Give the position of every leukocyte visible.
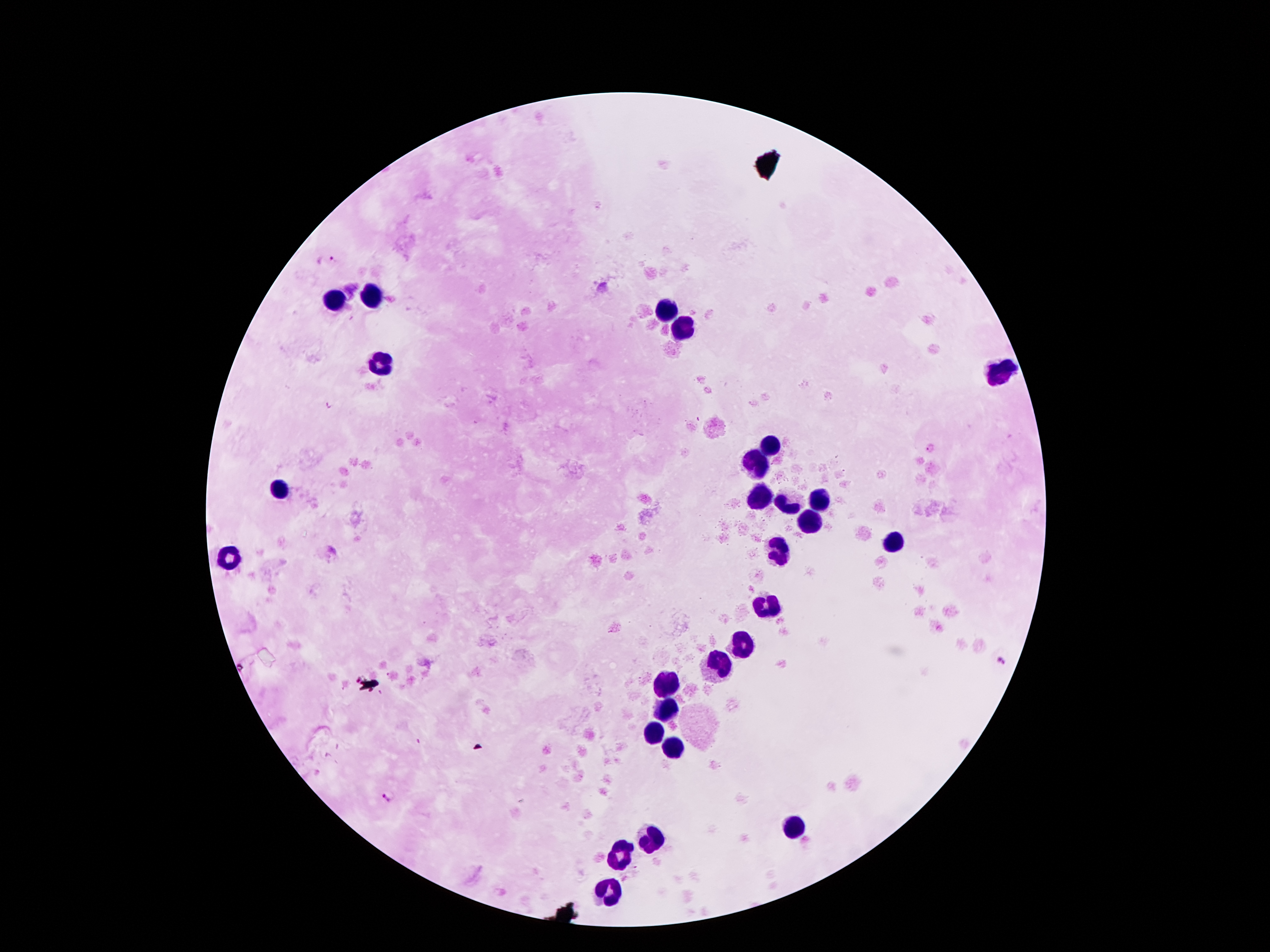

Approximate object centers, in pixels from the top-left corner.
Leukocytes: (x=371, y=295), (x=333, y=298), (x=663, y=311), (x=677, y=325), (x=379, y=363), (x=999, y=372), (x=774, y=447), (x=757, y=464), (x=283, y=489), (x=761, y=500), (x=818, y=501), (x=789, y=506), (x=810, y=522), (x=896, y=545), (x=780, y=554), (x=232, y=557), (x=766, y=607), (x=744, y=645), (x=717, y=663), (x=669, y=683), (x=665, y=705), (x=652, y=730), (x=669, y=747), (x=793, y=827), (x=650, y=839), (x=618, y=854), (x=608, y=898).

malaria parasite locations = (x=332, y=260), (x=1001, y=659), (x=387, y=798)
preparation = thick blood film
image size = 1270×952 pixels
magnification = 100x
capture = smartphone through the microscope eyepiece
field of view = single
stain = Giemsa
patient malaria status = positive for Plasmodium falciparum